Classify this cell by malaria status.
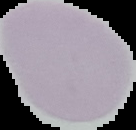

It is uninfected.

Cell region segmented out of the field of view; the surrounding area is masked to black. Image is 136×130 pixels. From a thin blood film.